Describe the morphology of the red blood cells.
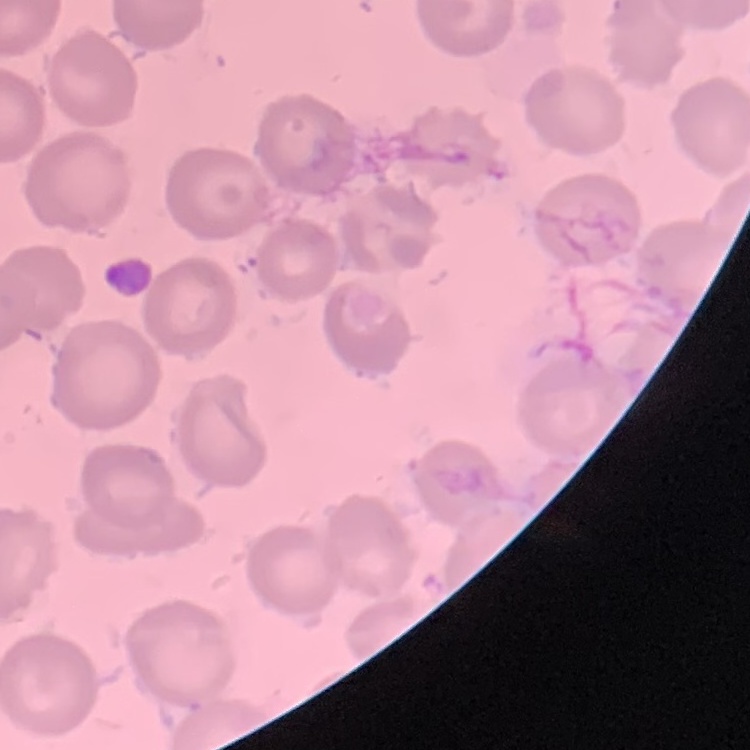

No rouleaux formation.

Summary:
  - Image type: one tile cut from a larger photomicrograph
  - Preparation: thin blood film
  - Stain: Field's or Giemsa